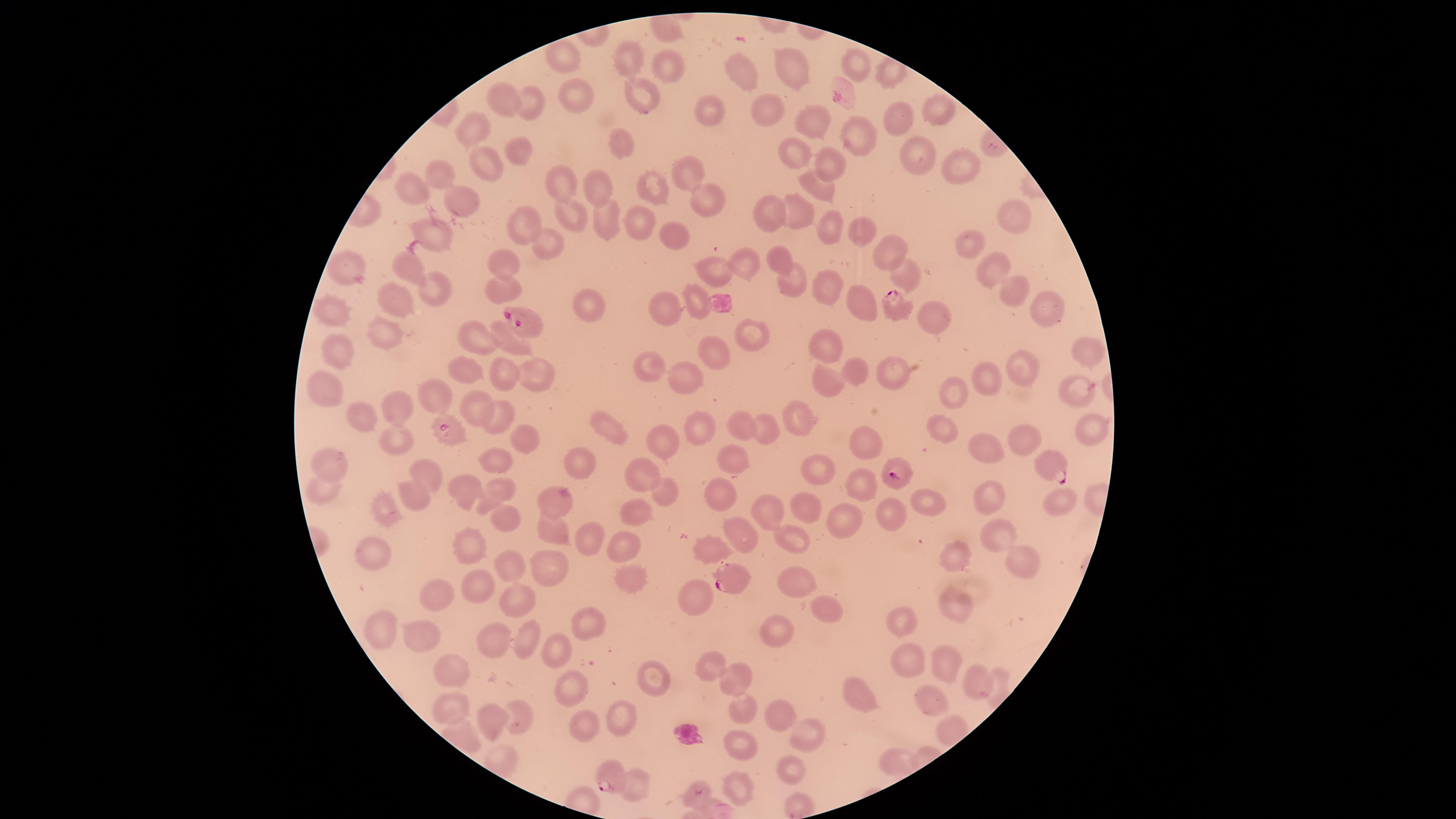

Approximate marker points, in pixels from the top-left corner. Parasitized red blood cells: (x=839, y=91), (x=892, y=304), (x=524, y=321), (x=449, y=429), (x=1052, y=466), (x=900, y=474), (x=728, y=576), (x=609, y=774), (x=698, y=793). Uninfected red blood cells: (x=636, y=50), (x=567, y=56), (x=666, y=63), (x=863, y=66), (x=796, y=70), (x=747, y=73), (x=577, y=90), (x=637, y=92), (x=539, y=100), (x=504, y=102), (x=765, y=105), (x=934, y=109), (x=706, y=111), (x=811, y=121), (x=901, y=123), (x=469, y=134), (x=855, y=137), (x=621, y=141), (x=523, y=152), (x=915, y=152), (x=794, y=155), (x=829, y=164), (x=944, y=164), (x=487, y=169), (x=432, y=170), (x=686, y=174), (x=595, y=185), (x=819, y=187), (x=656, y=189), (x=560, y=191), (x=414, y=195), (x=458, y=198), (x=702, y=199), (x=574, y=209), (x=764, y=210), (x=799, y=211), (x=1014, y=212), (x=642, y=217), (x=603, y=220), (x=831, y=226), (x=437, y=231), (x=523, y=231), (x=865, y=232), (x=678, y=238), (x=551, y=244), (x=975, y=244), (x=887, y=248), (x=774, y=255), (x=505, y=258), (x=743, y=262), (x=986, y=268), (x=408, y=269), (x=342, y=271), (x=715, y=271), (x=901, y=276), (x=788, y=285), (x=438, y=287), (x=502, y=287), (x=1013, y=289), (x=818, y=290), (x=690, y=299), (x=588, y=303), (x=664, y=303), (x=391, y=304), (x=867, y=304), (x=1041, y=306), (x=332, y=313), (x=937, y=318), (x=385, y=337), (x=750, y=338), (x=474, y=339), (x=829, y=341), (x=508, y=344), (x=1089, y=346), (x=338, y=347), (x=712, y=358), (x=856, y=366), (x=655, y=368), (x=1024, y=369), (x=533, y=373), (x=892, y=373), (x=469, y=376), (x=501, y=377), (x=677, y=377), (x=983, y=379), (x=827, y=381), (x=1076, y=387), (x=947, y=391), (x=437, y=398), (x=321, y=400), (x=478, y=402), (x=397, y=405), (x=795, y=412), (x=498, y=417), (x=606, y=425), (x=700, y=426), (x=747, y=426), (x=943, y=426), (x=1086, y=426), (x=767, y=429), (x=863, y=438), (x=519, y=440), (x=395, y=441), (x=1024, y=441), (x=519, y=443), (x=663, y=446), (x=986, y=453), (x=491, y=459), (x=732, y=459), (x=579, y=462), (x=330, y=467), (x=429, y=469), (x=824, y=472), (x=640, y=473), (x=864, y=476), (x=721, y=484), (x=468, y=489), (x=498, y=489), (x=322, y=490), (x=412, y=490), (x=662, y=494), (x=1062, y=497), (x=926, y=500), (x=989, y=501), (x=556, y=502), (x=558, y=502), (x=805, y=505), (x=382, y=510), (x=887, y=511), (x=633, y=512), (x=768, y=512), (x=843, y=518), (x=503, y=519), (x=550, y=527), (x=744, y=529), (x=995, y=533), (x=591, y=535), (x=792, y=536), (x=475, y=543), (x=620, y=546), (x=376, y=549), (x=711, y=549), (x=956, y=555), (x=1020, y=560), (x=548, y=564), (x=510, y=568), (x=625, y=572), (x=799, y=579), (x=481, y=586), (x=437, y=596), (x=697, y=598), (x=515, y=599), (x=957, y=608), (x=818, y=609), (x=902, y=622), (x=380, y=625), (x=583, y=626), (x=488, y=636), (x=422, y=637), (x=772, y=638), (x=523, y=640), (x=556, y=648), (x=904, y=658), (x=944, y=658), (x=710, y=667), (x=451, y=674), (x=647, y=675), (x=733, y=678), (x=974, y=678), (x=569, y=683), (x=856, y=696), (x=936, y=705), (x=454, y=706), (x=777, y=712), (x=496, y=714), (x=519, y=714), (x=742, y=715), (x=620, y=718), (x=578, y=719), (x=811, y=740), (x=743, y=751), (x=895, y=758), (x=794, y=768), (x=630, y=787), (x=740, y=788). Smartphone photograph through the microscope eyepiece. Circular visible region. Single field of view. Image is 1456×819 pixels. Presence: malaria parasites seen. Thin blood film. Species: Plasmodium falciparum. Giemsa-stained preparation.